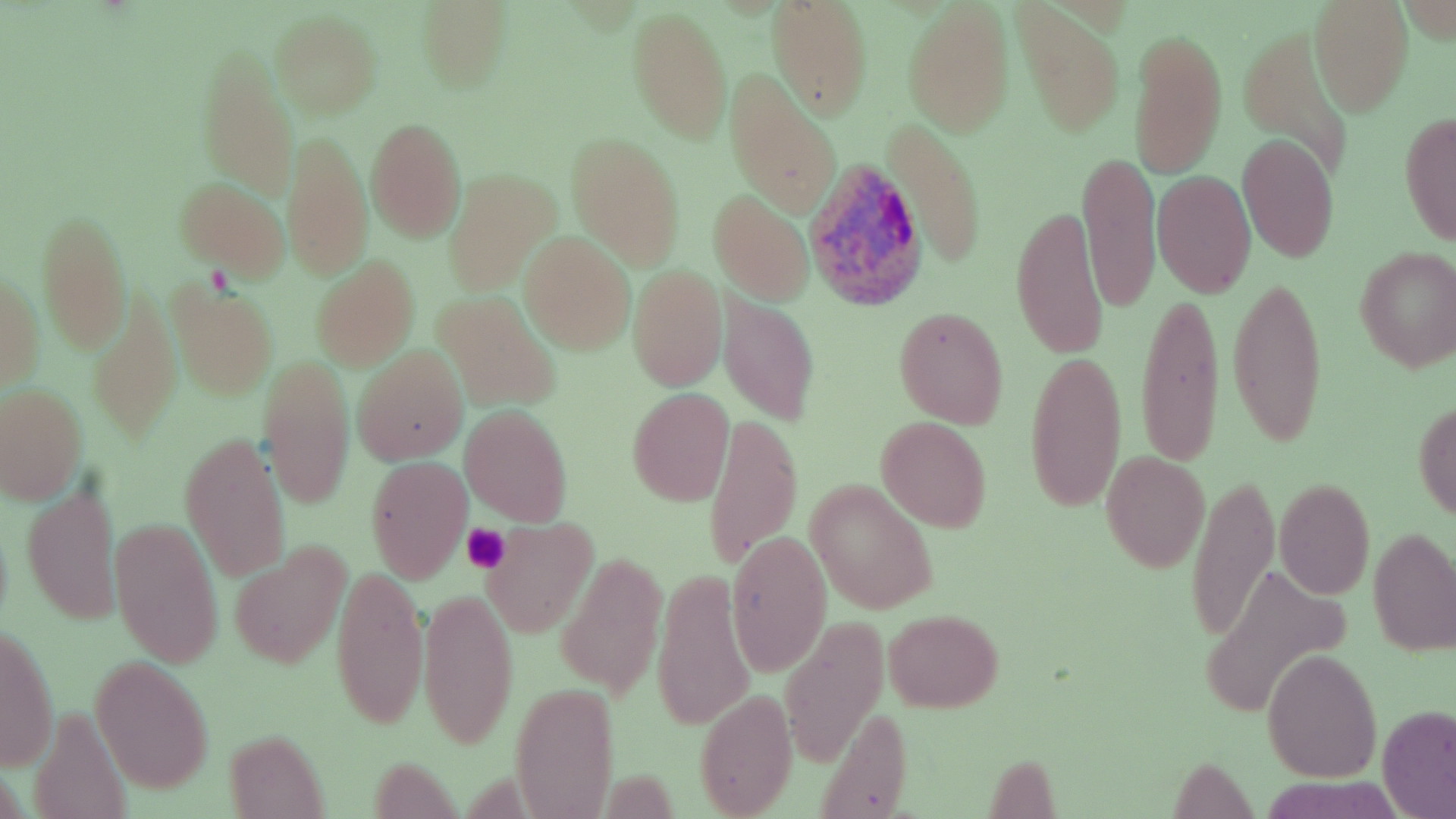

Summary:
  - Coordinate format: approximate bounding boxes as named x1/y1/x2/y2 corners in pixels
  - Platelet locations: (x1=460, y1=525, x2=511, y2=573)
  - Plasmodium ovale-infected red blood cell locations: (x1=805, y1=159, x2=928, y2=313)
  - Uninfected red blood cell locations: (x1=416, y1=1, x2=512, y2=91), (x1=1309, y1=1, x2=1413, y2=115), (x1=764, y1=2, x2=873, y2=120), (x1=903, y1=3, x2=1013, y2=137), (x1=1014, y1=5, x2=1124, y2=138), (x1=628, y1=7, x2=732, y2=146), (x1=270, y1=13, x2=381, y2=117), (x1=1130, y1=24, x2=1227, y2=181), (x1=1238, y1=27, x2=1361, y2=183), (x1=197, y1=51, x2=298, y2=198), (x1=724, y1=76, x2=840, y2=216), (x1=1398, y1=109, x2=1456, y2=247), (x1=365, y1=118, x2=466, y2=243), (x1=888, y1=120, x2=988, y2=271), (x1=283, y1=129, x2=373, y2=281), (x1=566, y1=133, x2=684, y2=270), (x1=1238, y1=133, x2=1338, y2=263), (x1=1078, y1=149, x2=1159, y2=316), (x1=445, y1=169, x2=558, y2=296), (x1=1153, y1=171, x2=1256, y2=296), (x1=174, y1=179, x2=289, y2=281), (x1=710, y1=190, x2=813, y2=305), (x1=1011, y1=202, x2=1110, y2=364), (x1=36, y1=208, x2=130, y2=354), (x1=520, y1=232, x2=636, y2=354), (x1=1354, y1=247, x2=1456, y2=372), (x1=312, y1=257, x2=419, y2=370), (x1=627, y1=266, x2=725, y2=392), (x1=0, y1=267, x2=43, y2=392), (x1=1227, y1=271, x2=1330, y2=453), (x1=168, y1=281, x2=277, y2=398), (x1=88, y1=288, x2=181, y2=441), (x1=1137, y1=290, x2=1225, y2=470), (x1=435, y1=292, x2=560, y2=411), (x1=718, y1=297, x2=820, y2=425), (x1=892, y1=307, x2=1009, y2=429), (x1=352, y1=345, x2=468, y2=464), (x1=1023, y1=350, x2=1128, y2=514), (x1=260, y1=353, x2=355, y2=512), (x1=0, y1=384, x2=85, y2=502), (x1=627, y1=388, x2=734, y2=507), (x1=1412, y1=400, x2=1456, y2=521), (x1=460, y1=406, x2=573, y2=526), (x1=702, y1=408, x2=802, y2=572), (x1=875, y1=416, x2=991, y2=531), (x1=179, y1=430, x2=288, y2=584), (x1=1102, y1=452, x2=1208, y2=572), (x1=366, y1=456, x2=471, y2=582), (x1=1185, y1=474, x2=1277, y2=646), (x1=1275, y1=479, x2=1373, y2=600), (x1=805, y1=480, x2=939, y2=615), (x1=23, y1=483, x2=119, y2=625), (x1=111, y1=518, x2=222, y2=668), (x1=480, y1=519, x2=597, y2=637), (x1=1368, y1=528, x2=1456, y2=655), (x1=726, y1=530, x2=831, y2=676), (x1=230, y1=544, x2=350, y2=670), (x1=557, y1=556, x2=667, y2=697), (x1=331, y1=563, x2=429, y2=731), (x1=1202, y1=563, x2=1352, y2=717), (x1=651, y1=568, x2=754, y2=734), (x1=417, y1=586, x2=516, y2=751), (x1=886, y1=609, x2=1001, y2=712), (x1=780, y1=617, x2=885, y2=762), (x1=1, y1=626, x2=59, y2=772), (x1=1262, y1=650, x2=1381, y2=780), (x1=92, y1=659, x2=213, y2=793), (x1=510, y1=683, x2=619, y2=819), (x1=695, y1=690, x2=797, y2=818), (x1=29, y1=701, x2=135, y2=819), (x1=815, y1=703, x2=916, y2=816), (x1=1375, y1=707, x2=1455, y2=818), (x1=223, y1=730, x2=328, y2=816), (x1=1167, y1=759, x2=1257, y2=814)
  - Slide-level diagnosis: Plasmodium ovale
  - Stain: May-Grünwald-Giemsa
  - Magnification: 1000x
  - Preparation: thin blood smear
  - Modality: light microscopy
  - Image size: 1456×819 pixels
  - Field of view: single